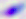

{
  "identification": "Toxoplasma gondii",
  "modality": "photomicrograph",
  "magnification": "400x"
}